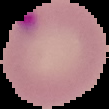
{
  "image_type": "segmented cell region on a black background",
  "preparation": "thin blood film",
  "malaria_status": "parasitized",
  "image_size": "109×109 pixels"
}